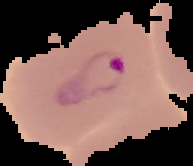
Summary:
  - Result: Plasmodium parasites identified
  - Preparation: thin blood smear
  - Image type: segmented cell region on a black background
  - Image size: 193×166 pixels